Classify this cell by malaria status.
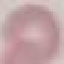

It is uninfected.

Summary:
  - Preparation: thin smear
  - Image type: automatically extracted cell patch, resized to 64 × 64 pixels
  - Capture: smartphone camera at the microscope eyepiece
  - Stain: Giemsa